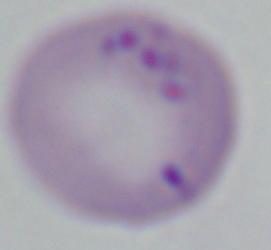
magnification = 1000x
identification = Babesia
modality = micrograph